Report the malaria status of this cell.
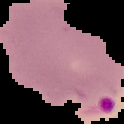
It is parasitized.

Summary:
  - Preparation: thin blood smear
  - Image size: 124×124 pixels
  - Image type: cell region segmented out of the field of view; surrounding area masked to black